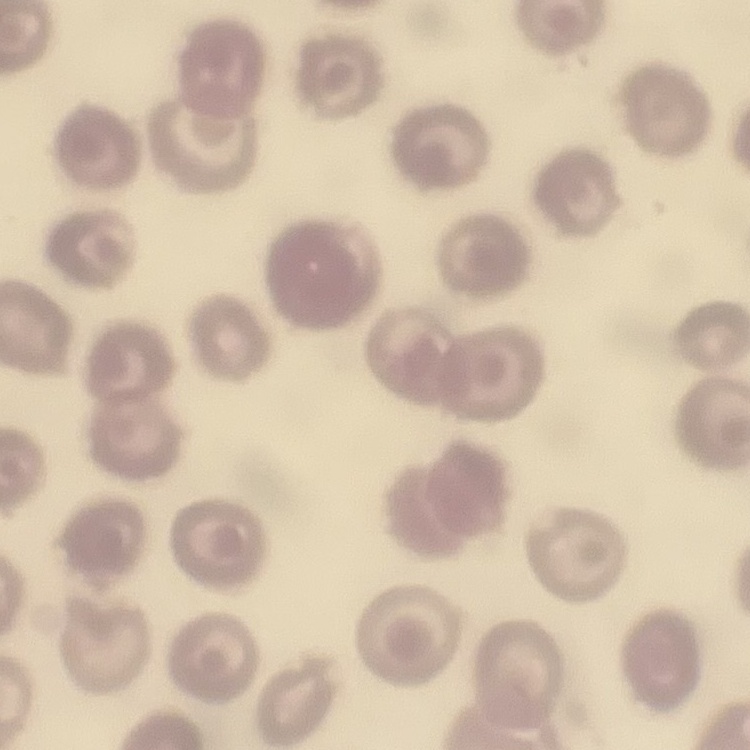

Summary:
  - Red blood cell morphology: no rouleaux formation
  - Stain: Field's or Giemsa
  - Preparation: thin blood smear
  - Image type: square crop of a larger photomicrograph